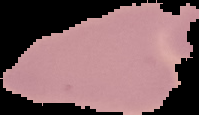

Summary:
  - Result: no malaria parasites detected
  - Image type: segmented cell region on a black background
  - Preparation: thin blood smear
  - Image size: 199×115 pixels